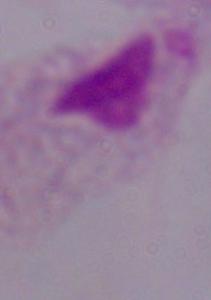

identification: trichomonad
modality: micrograph
magnification: 1000x